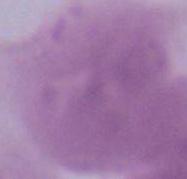

identification = erythrocyte
magnification = 1000x
modality = micrograph